Outline each blood parasite and name the species.
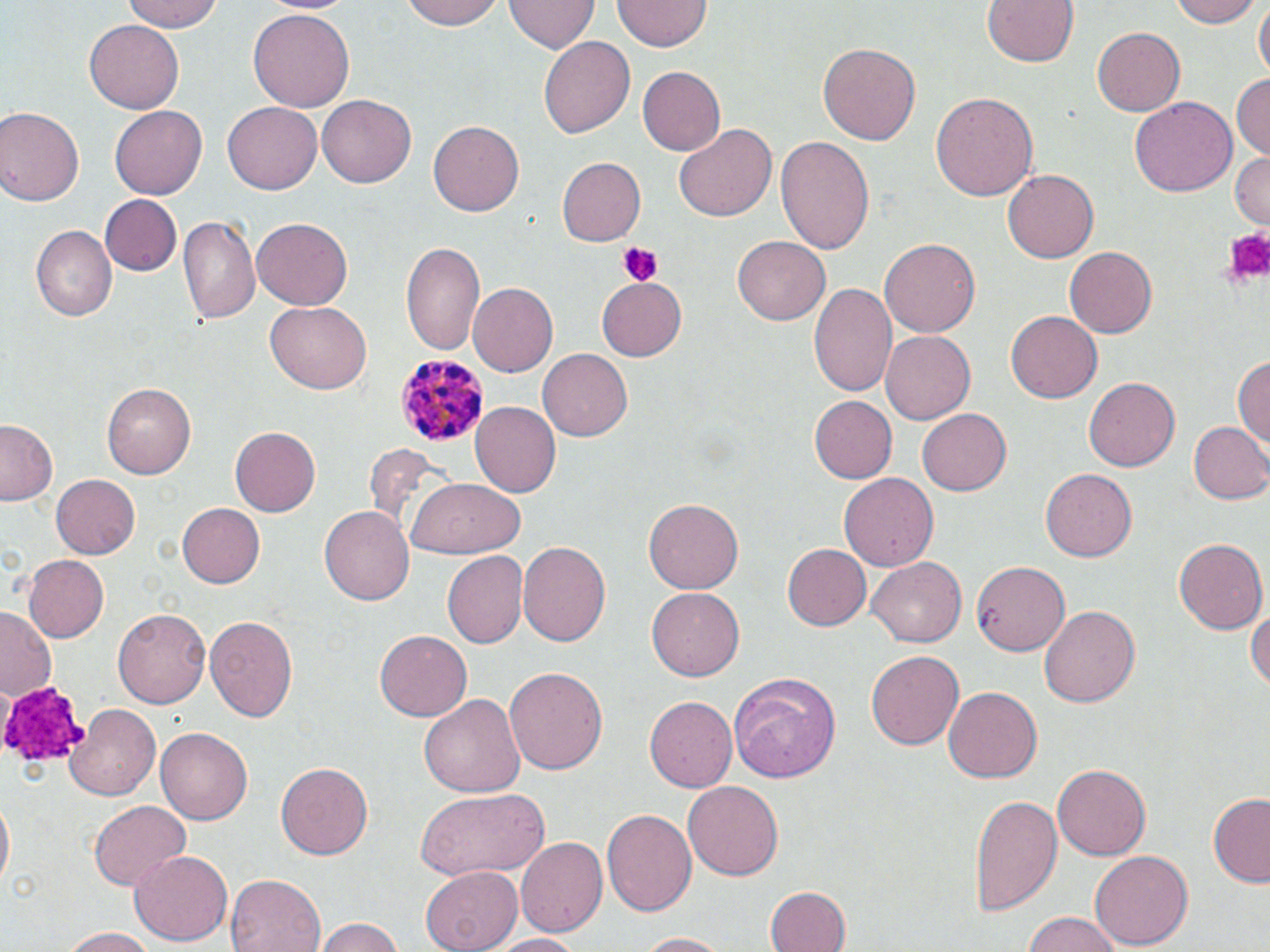
Approximate bounding boxes as named x1/y1/x2/y2 corners in pixels.
Plasmodium malariae-infected red blood cells: (x1=396, y1=354, x2=490, y2=448).
No Plasmodium falciparum, Plasmodium ovale, Plasmodium vivax, Babesia divergens, or Trypanosoma brucei observed.

Summary:
  - Platelet locations: (x1=1221, y1=224, x2=1270, y2=285), (x1=617, y1=243, x2=661, y2=286), (x1=1, y1=680, x2=89, y2=765)
  - Uninfected red blood cell locations: (x1=119, y1=0, x2=226, y2=32), (x1=259, y1=0, x2=359, y2=16), (x1=405, y1=0, x2=506, y2=29), (x1=507, y1=0, x2=597, y2=54), (x1=613, y1=0, x2=709, y2=52), (x1=981, y1=0, x2=1081, y2=68), (x1=1173, y1=0, x2=1260, y2=27), (x1=1254, y1=3, x2=1268, y2=84), (x1=249, y1=10, x2=356, y2=112), (x1=85, y1=20, x2=185, y2=113), (x1=1091, y1=27, x2=1184, y2=116), (x1=540, y1=35, x2=635, y2=140), (x1=819, y1=43, x2=920, y2=146), (x1=637, y1=67, x2=725, y2=154), (x1=1232, y1=71, x2=1270, y2=157), (x1=930, y1=92, x2=1040, y2=201), (x1=317, y1=96, x2=416, y2=187), (x1=1129, y1=97, x2=1236, y2=196), (x1=223, y1=101, x2=323, y2=194), (x1=109, y1=104, x2=207, y2=199), (x1=0, y1=107, x2=82, y2=208), (x1=428, y1=119, x2=524, y2=217), (x1=672, y1=124, x2=776, y2=222), (x1=775, y1=134, x2=877, y2=252), (x1=1228, y1=150, x2=1270, y2=229), (x1=556, y1=158, x2=646, y2=246), (x1=1003, y1=169, x2=1098, y2=263), (x1=97, y1=195, x2=180, y2=276), (x1=179, y1=217, x2=260, y2=323), (x1=250, y1=217, x2=352, y2=310), (x1=29, y1=228, x2=115, y2=322), (x1=734, y1=236, x2=831, y2=325), (x1=399, y1=238, x2=486, y2=354), (x1=881, y1=240, x2=979, y2=337), (x1=1065, y1=246, x2=1160, y2=338), (x1=597, y1=277, x2=688, y2=361), (x1=468, y1=282, x2=558, y2=377), (x1=808, y1=282, x2=897, y2=399), (x1=265, y1=301, x2=371, y2=395), (x1=1006, y1=310, x2=1102, y2=403), (x1=880, y1=330, x2=974, y2=424), (x1=538, y1=350, x2=632, y2=440), (x1=1233, y1=353, x2=1269, y2=454), (x1=1085, y1=376, x2=1180, y2=473), (x1=103, y1=380, x2=197, y2=478), (x1=807, y1=395, x2=897, y2=484), (x1=469, y1=402, x2=560, y2=498), (x1=916, y1=408, x2=1011, y2=496), (x1=1, y1=420, x2=61, y2=506), (x1=1188, y1=421, x2=1270, y2=504), (x1=230, y1=426, x2=321, y2=518), (x1=360, y1=445, x2=459, y2=541), (x1=1040, y1=468, x2=1136, y2=562), (x1=48, y1=472, x2=139, y2=560), (x1=839, y1=473, x2=939, y2=571), (x1=408, y1=479, x2=521, y2=559), (x1=643, y1=499, x2=744, y2=594), (x1=174, y1=501, x2=266, y2=589), (x1=319, y1=506, x2=415, y2=605), (x1=1172, y1=538, x2=1265, y2=633), (x1=516, y1=543, x2=611, y2=651), (x1=783, y1=544, x2=871, y2=631), (x1=440, y1=550, x2=527, y2=650), (x1=22, y1=554, x2=109, y2=642), (x1=866, y1=557, x2=964, y2=648), (x1=973, y1=561, x2=1069, y2=657), (x1=645, y1=586, x2=745, y2=682), (x1=1248, y1=600, x2=1270, y2=698), (x1=1038, y1=605, x2=1138, y2=709), (x1=114, y1=608, x2=210, y2=708), (x1=0, y1=609, x2=60, y2=699), (x1=202, y1=616, x2=300, y2=723), (x1=373, y1=630, x2=471, y2=721), (x1=866, y1=650, x2=964, y2=751), (x1=506, y1=666, x2=608, y2=777), (x1=729, y1=673, x2=842, y2=783), (x1=942, y1=686, x2=1041, y2=784), (x1=419, y1=695, x2=525, y2=798), (x1=644, y1=696, x2=736, y2=792), (x1=66, y1=703, x2=160, y2=798), (x1=155, y1=728, x2=250, y2=825), (x1=276, y1=762, x2=374, y2=860), (x1=1053, y1=762, x2=1151, y2=860), (x1=682, y1=781, x2=785, y2=881), (x1=415, y1=787, x2=549, y2=881), (x1=967, y1=793, x2=1062, y2=914), (x1=1207, y1=794, x2=1270, y2=885), (x1=0, y1=795, x2=14, y2=887), (x1=88, y1=799, x2=191, y2=893), (x1=602, y1=807, x2=698, y2=917), (x1=516, y1=835, x2=607, y2=940), (x1=130, y1=848, x2=232, y2=945), (x1=1088, y1=851, x2=1194, y2=951), (x1=421, y1=865, x2=523, y2=951), (x1=227, y1=874, x2=326, y2=952), (x1=765, y1=886, x2=852, y2=952), (x1=1019, y1=913, x2=1127, y2=952), (x1=311, y1=915, x2=408, y2=952), (x1=60, y1=926, x2=158, y2=951), (x1=635, y1=931, x2=729, y2=951), (x1=485, y1=932, x2=587, y2=952)
  - Slide-level diagnosis: Plasmodium malariae
  - Modality: optical microscopy
  - Field of view: one of a larger specimen
  - Preparation: thin blood smear
  - Stain: May-Grünwald-Giemsa
  - Magnification: 1000x
  - Image size: 1270×952 pixels